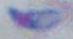
Toxoplasma gondii is seen. 1000x magnification. Micrograph.